Classify this cell by malaria status.
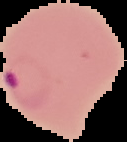
It is parasitized.

image size = 127×142 pixels
preparation = thin blood film
image type = segmented cell region on a black background